State which parasite is depicted.
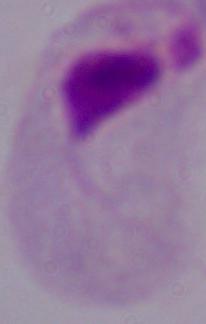

This is a trichomonad.

modality = photomicrograph
magnification = 1000x